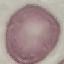
Result: no malaria parasites detected. Cell patch, automatically extracted from a larger field of view and resized to 64 × 64 pixels. Giemsa stain. Thin blood film. Acquired by smartphone through the microscope eyepiece.